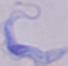
Summary:
  - Magnification: 1000x
  - Modality: photomicrograph
  - Identification: trypanosome